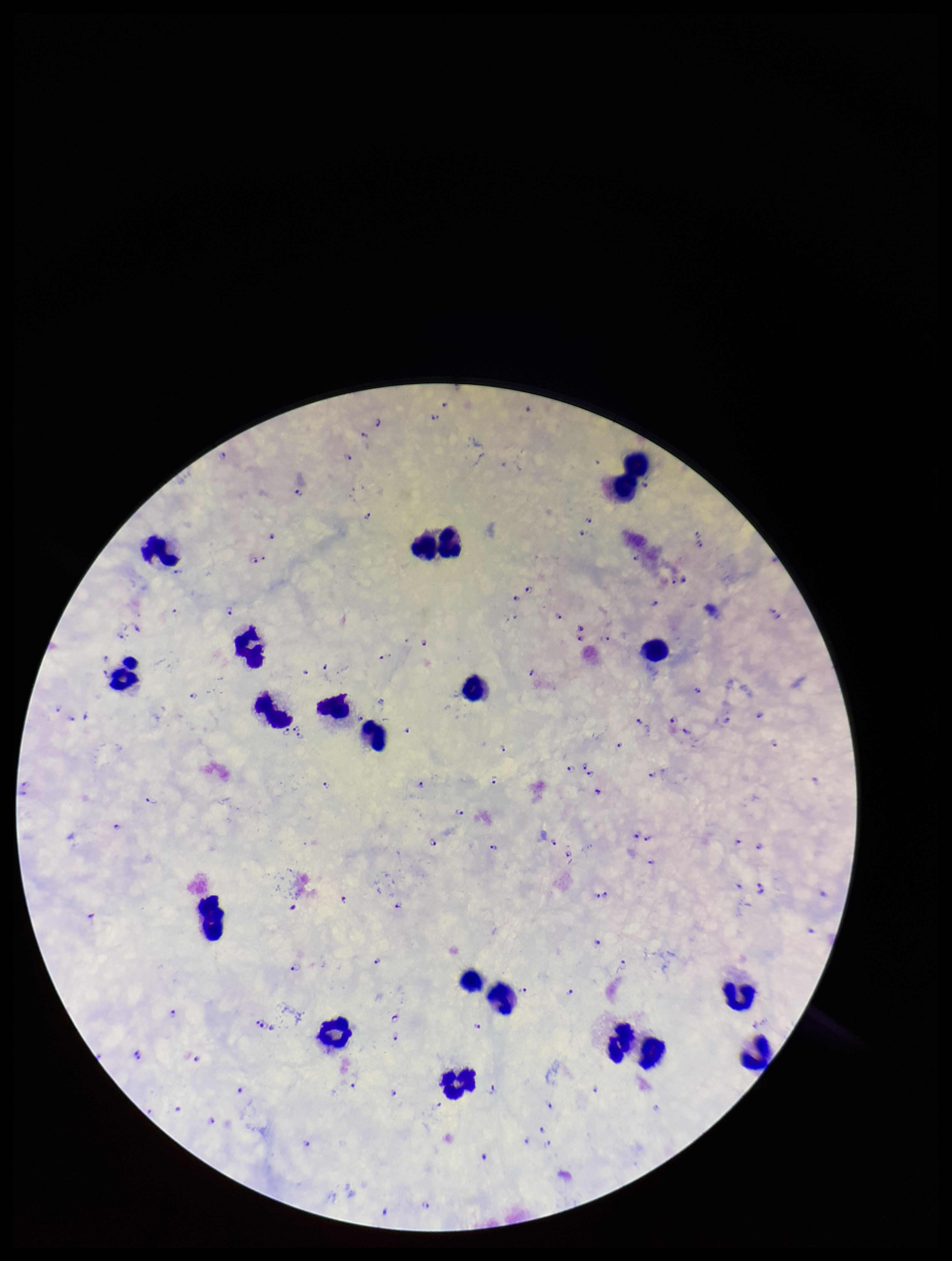

capture = smartphone photograph through the microscope eyepiece
parasite count = 122
leukocyte count = 22
field of view = single
image size = 952×1261 pixels
species reported for this patient = Plasmodium falciparum
preparation = thick blood smear
Plasmodium parasites = detected
patient malaria status = infected
stain = Giemsa